State the preparation type.
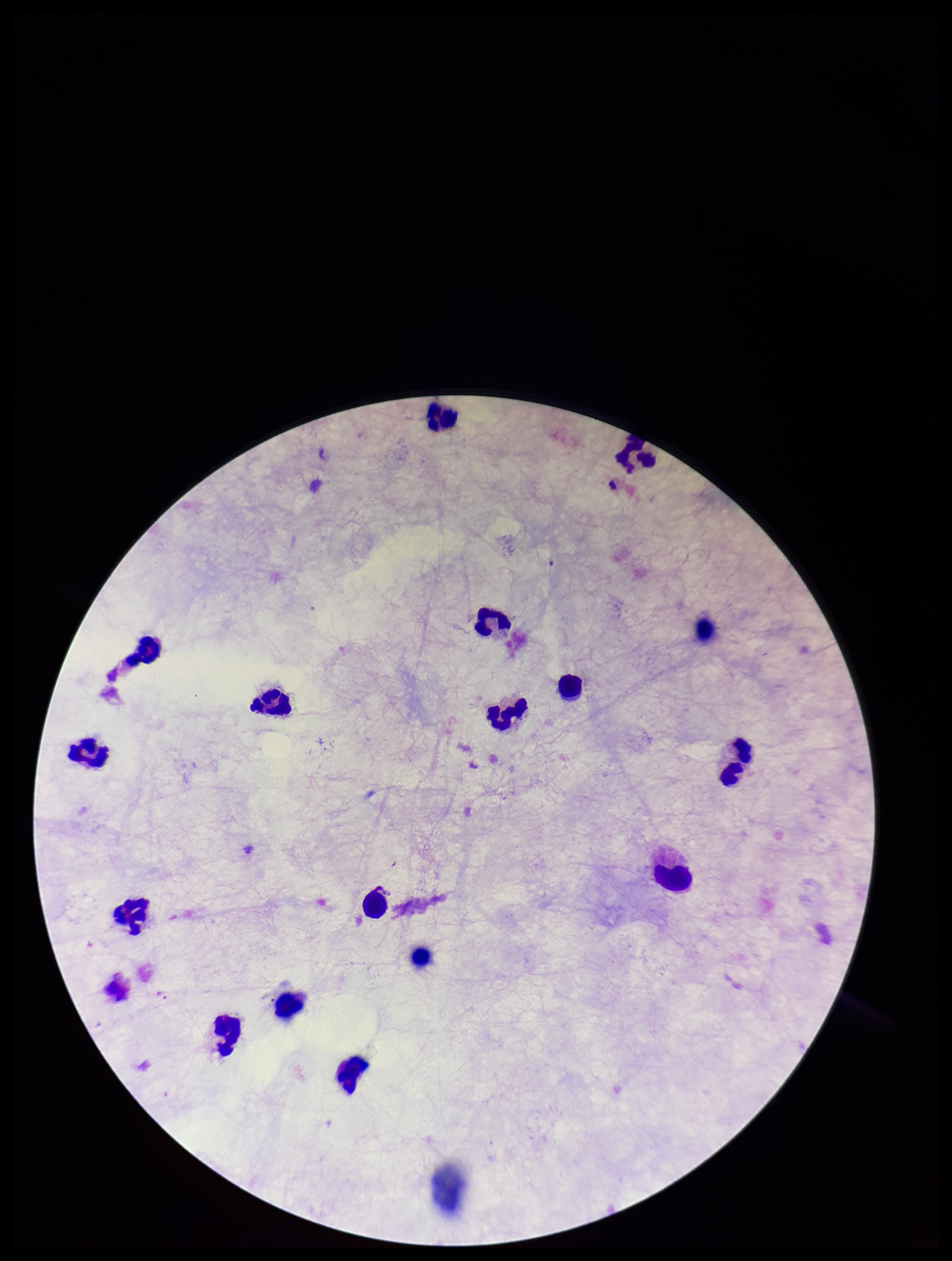

It is a thick blood smear.

patient_malaria_status: negative
plasmodium_parasites: none seen
image_size: 952×1261 pixels
stain: Giemsa
parasite_count: 0
leukocyte_count: 16
field_of_view: single
capture: smartphone photograph through the microscope eyepiece